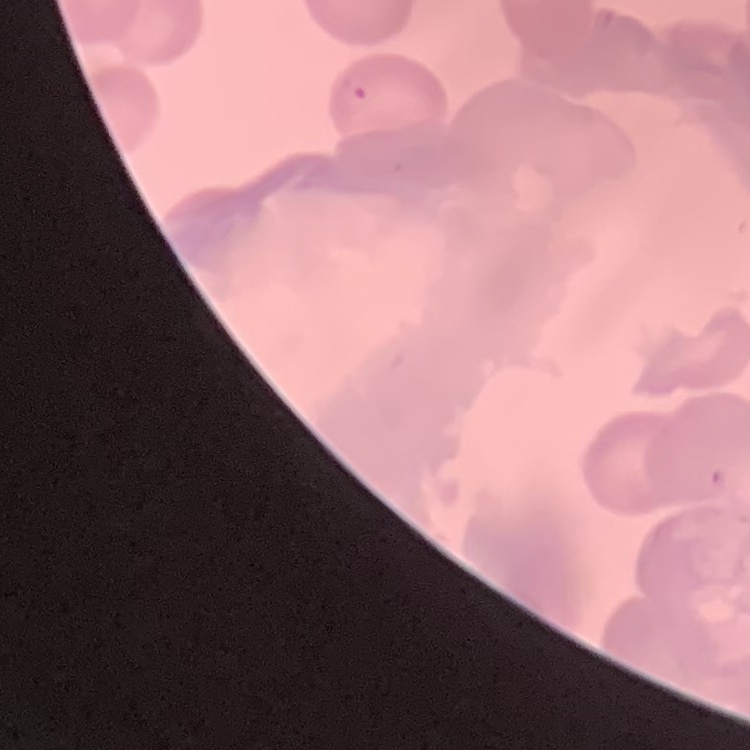
{
  "erythrocyte_morphology": "no rouleaux formation",
  "image_type": "one tile cut from a larger photomicrograph",
  "stain": "Field's or Giemsa",
  "preparation": "thin blood smear"
}